Describe the morphology of the erythrocytes.
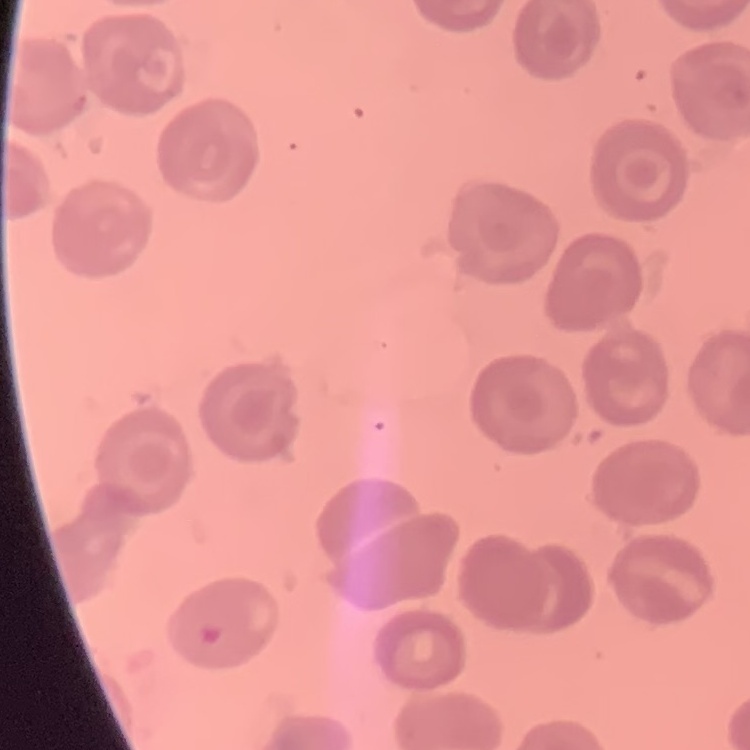
They show no rouleaux formation.

Summary:
  - Stain: Field's or Giemsa
  - Image type: square crop of a larger photomicrograph
  - Preparation: thin blood film